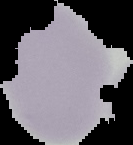

image type = cell region segmented out of the field of view; surrounding area masked to black
result = negative for Plasmodium parasites
image size = 133×145 pixels
preparation = thin blood smear